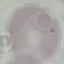
Summary:
  - Malaria status: uninfected
  - Stain: Giemsa
  - Preparation: thin smear
  - Image type: cell patch, automatically extracted from a larger field of view and resized to 64 × 64 pixels
  - Capture: smartphone through the microscope eyepiece